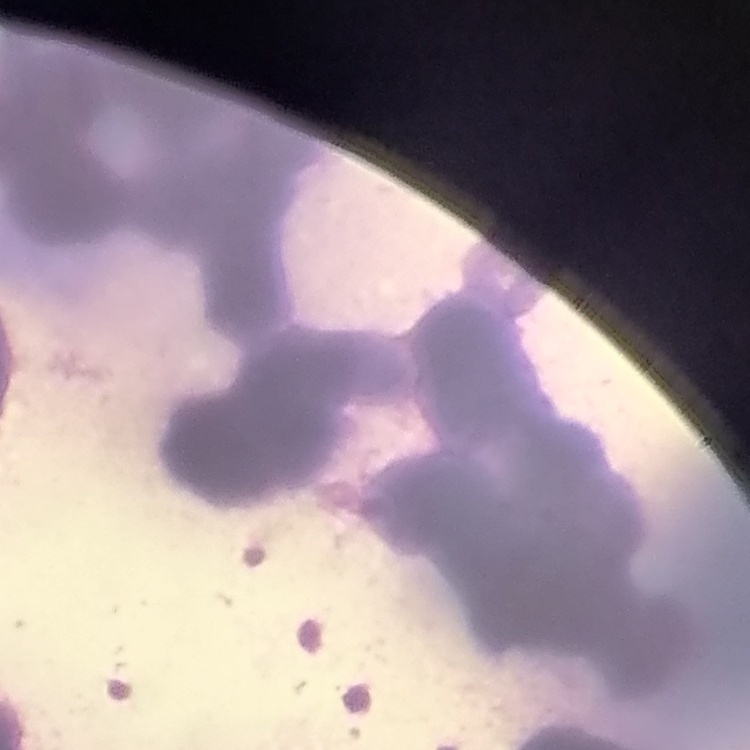

erythrocyte morphology = rouleaux formation
preparation = thin peripheral smear
image type = one tile cut from a larger photomicrograph
stain = Field's or Giemsa